State which cell type is depicted.
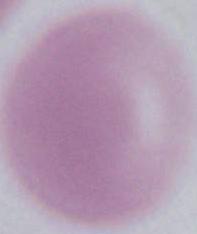

An erythrocyte.

magnification: 1000x
modality: micrograph